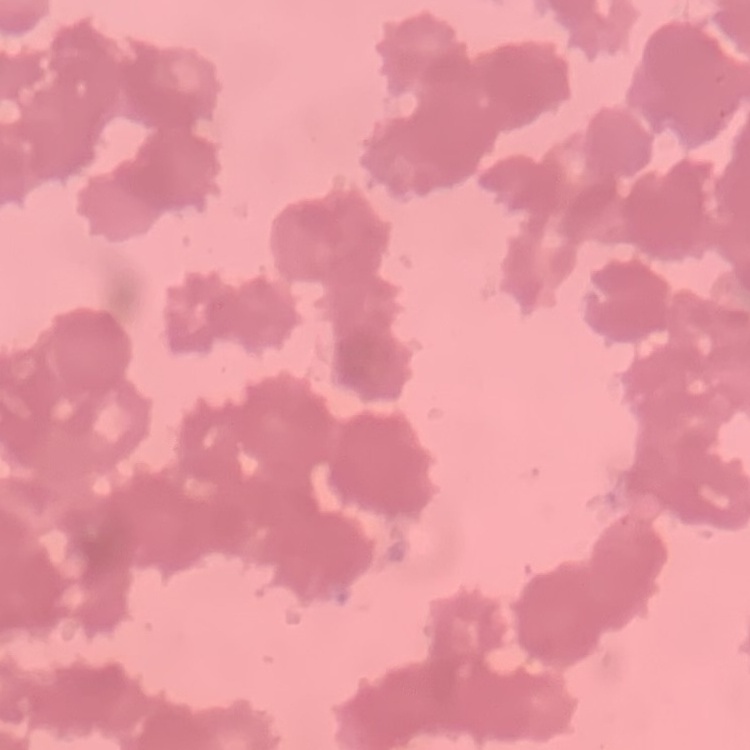

Summary:
  - Red blood cell morphology: rouleaux formation
  - Stain: Field's or Giemsa
  - Image type: square crop of a larger photomicrograph
  - Preparation: thin peripheral smear